Report the malaria status of this cell.
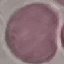

Uninfected.

preparation = thin blood film
stain = Giemsa
capture = smartphone through the microscope eyepiece
image type = cell patch, automatically extracted from a larger field of view and resized to 64 × 64 pixels